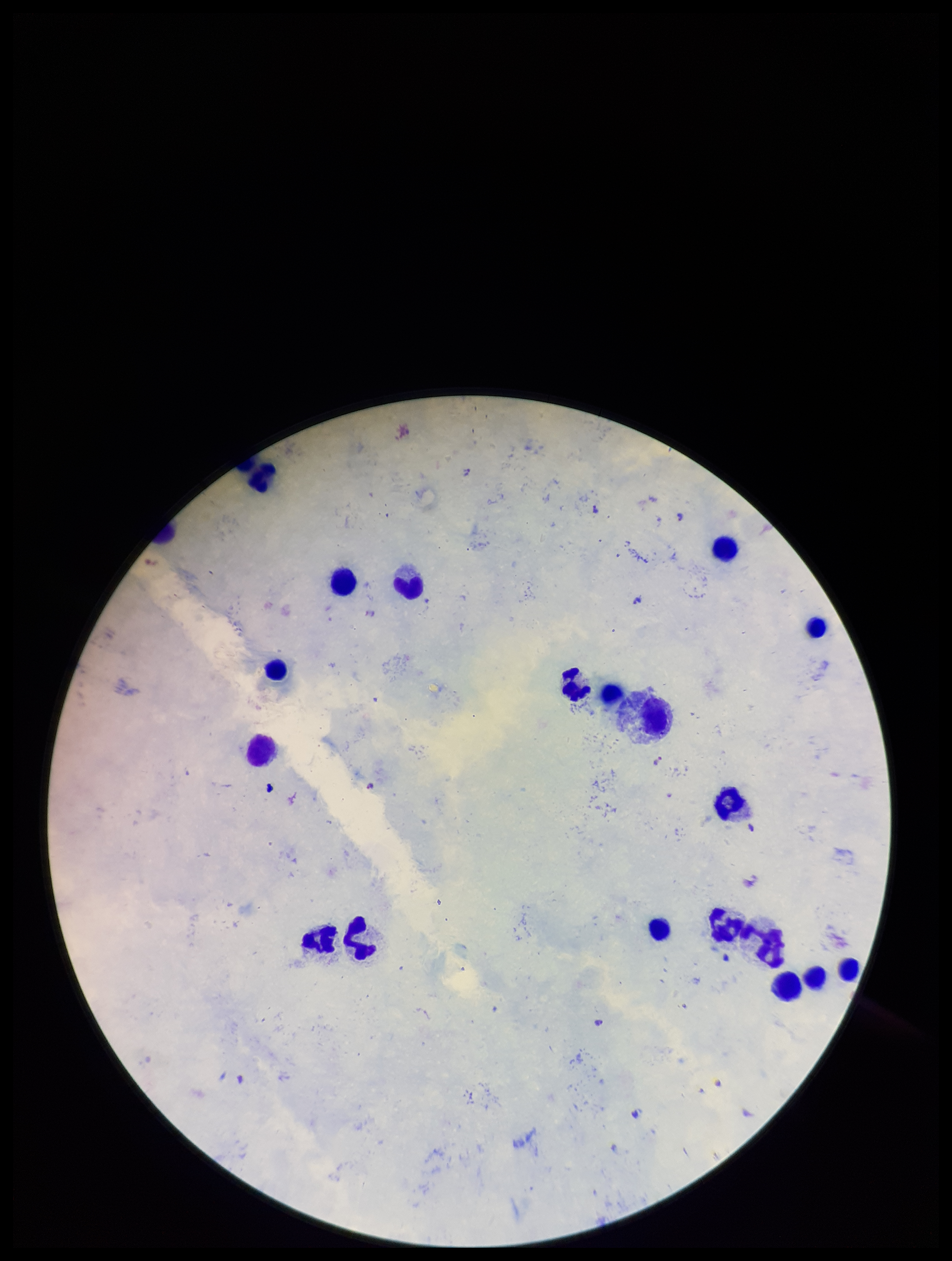

Summary:
  - Stain: Giemsa
  - Capture: smartphone photograph through the microscope eyepiece
  - Parasite count: 5
  - Field of view: one from this slide
  - Preparation: thick
  - Image size: 952×1261 pixels
  - Plasmodium parasites: seen
  - Leukocyte count: 18
  - Species reported for this patient: Plasmodium falciparum
  - Patient malaria status: infected